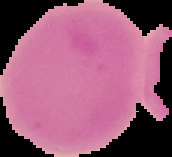
{
  "image_size": "172×157 pixels",
  "preparation": "thin blood smear",
  "malaria_status": "uninfected",
  "image_type": "segmented cell region on a black background"
}